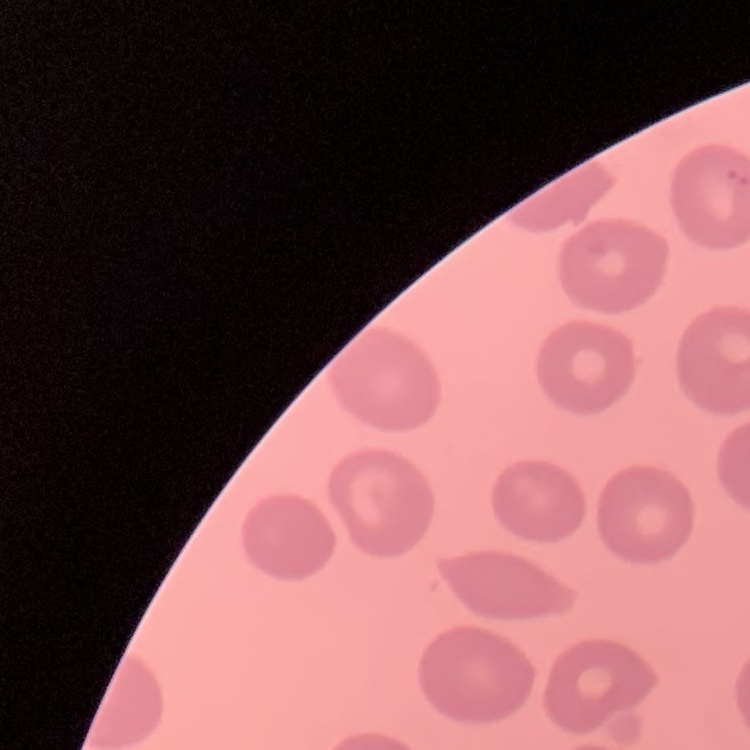
The erythrocytes show no rouleaux formation. Stained with either Field's or Giemsa. Thin peripheral smear. Square crop of a larger photomicrograph.